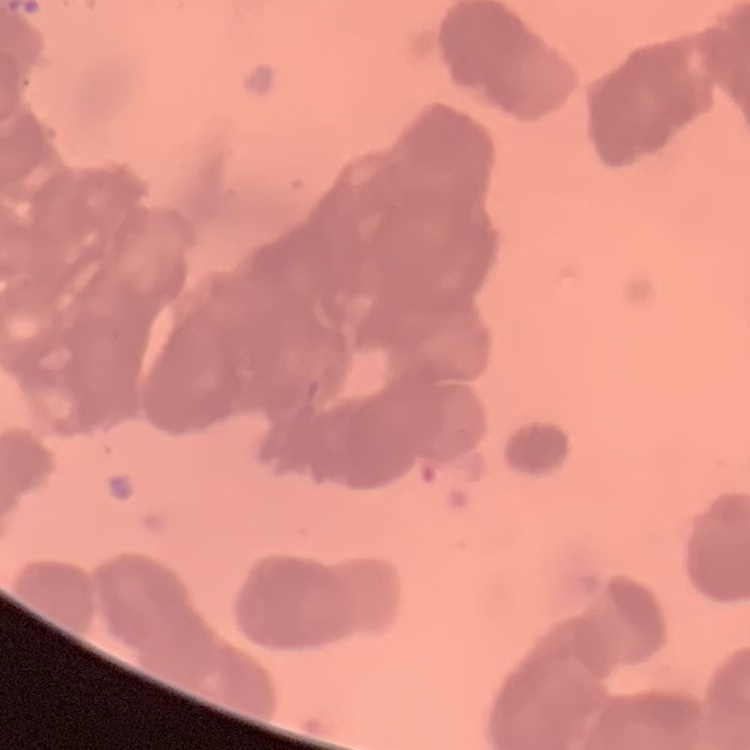
{
  "red_blood_cell_morphology": "rouleaux formation",
  "image_type": "square crop of a larger photomicrograph",
  "stain": "Field's or Giemsa",
  "preparation": "thin blood film"
}